Name the parasite shown.
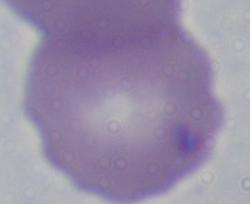

This is Babesia.

Summary:
  - Modality: photomicrograph
  - Magnification: 1000x